Report the malaria status of this cell.
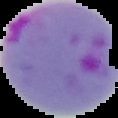
Parasitized.

From a thin blood smear. Image is 118×118 pixels. Cell region segmented out of the field of view; the surrounding area is masked to black.